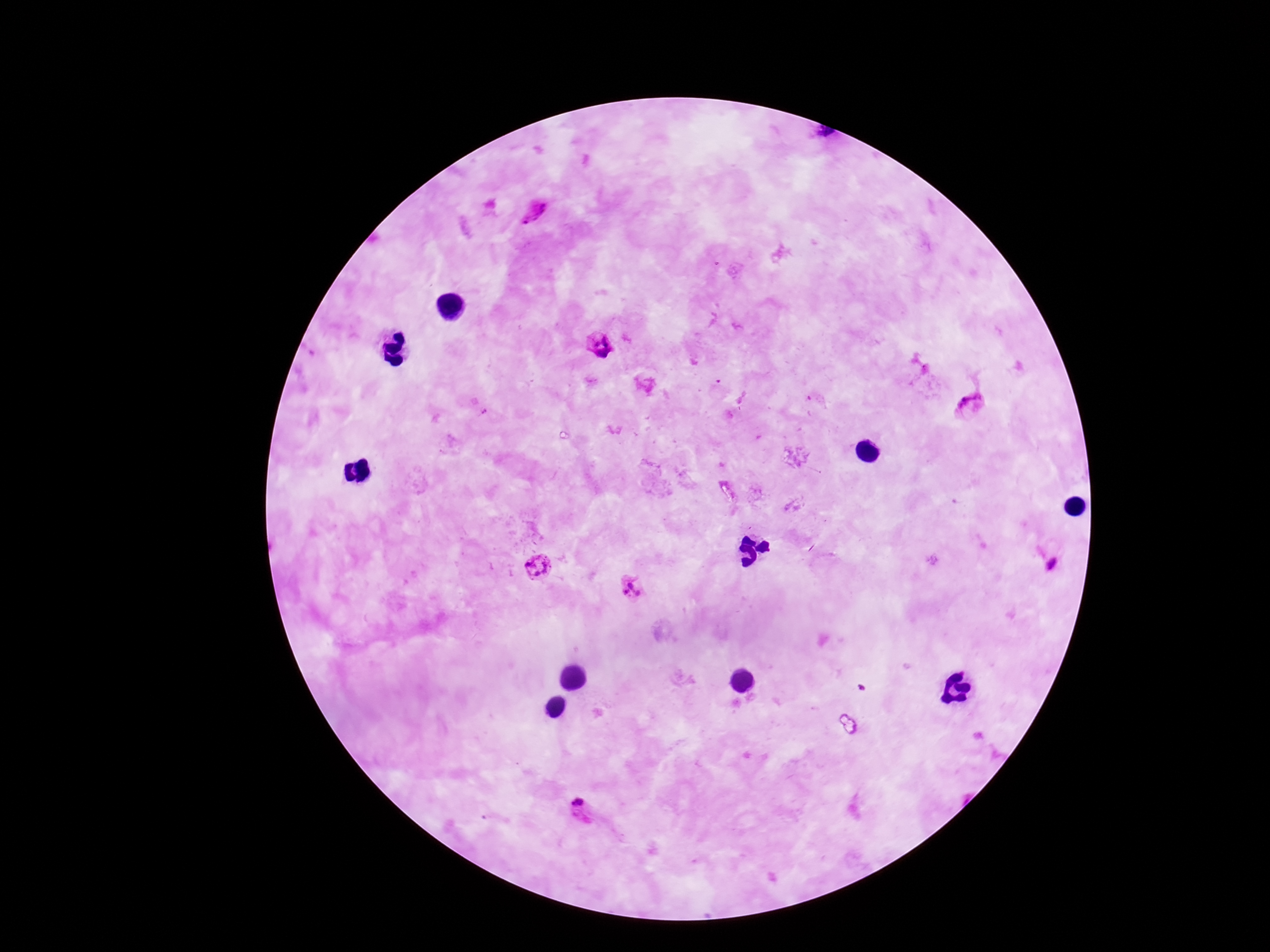
Approximate object centers, in pixels from the top-left corner.
Summary:
  - Plasmodium parasite locations: (x=537, y=213), (x=599, y=345), (x=972, y=407), (x=1051, y=566), (x=539, y=569), (x=632, y=588), (x=578, y=802)
  - Capture: smartphone camera through the microscope eyepiece
  - Patient malaria status: infected
  - Preparation: thick blood film
  - Magnification: 100x
  - Stain: Giemsa
  - Field of view: one from this slide
  - Image size: 1270×952 pixels